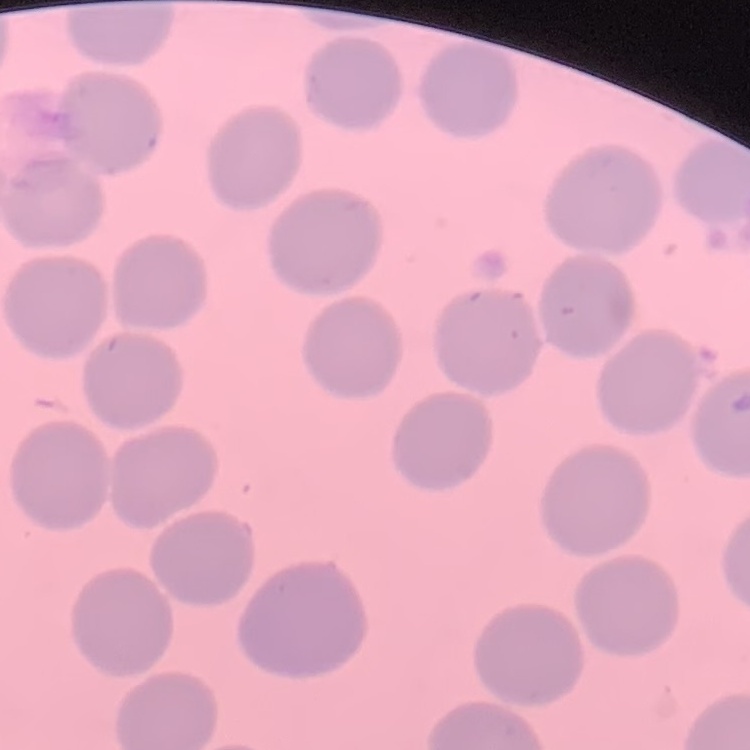

The erythrocytes exhibit no rouleaux formation. One tile cut from a larger photomicrograph. Thin blood film. Field's or Giemsa stain.